Identify the preparation type.
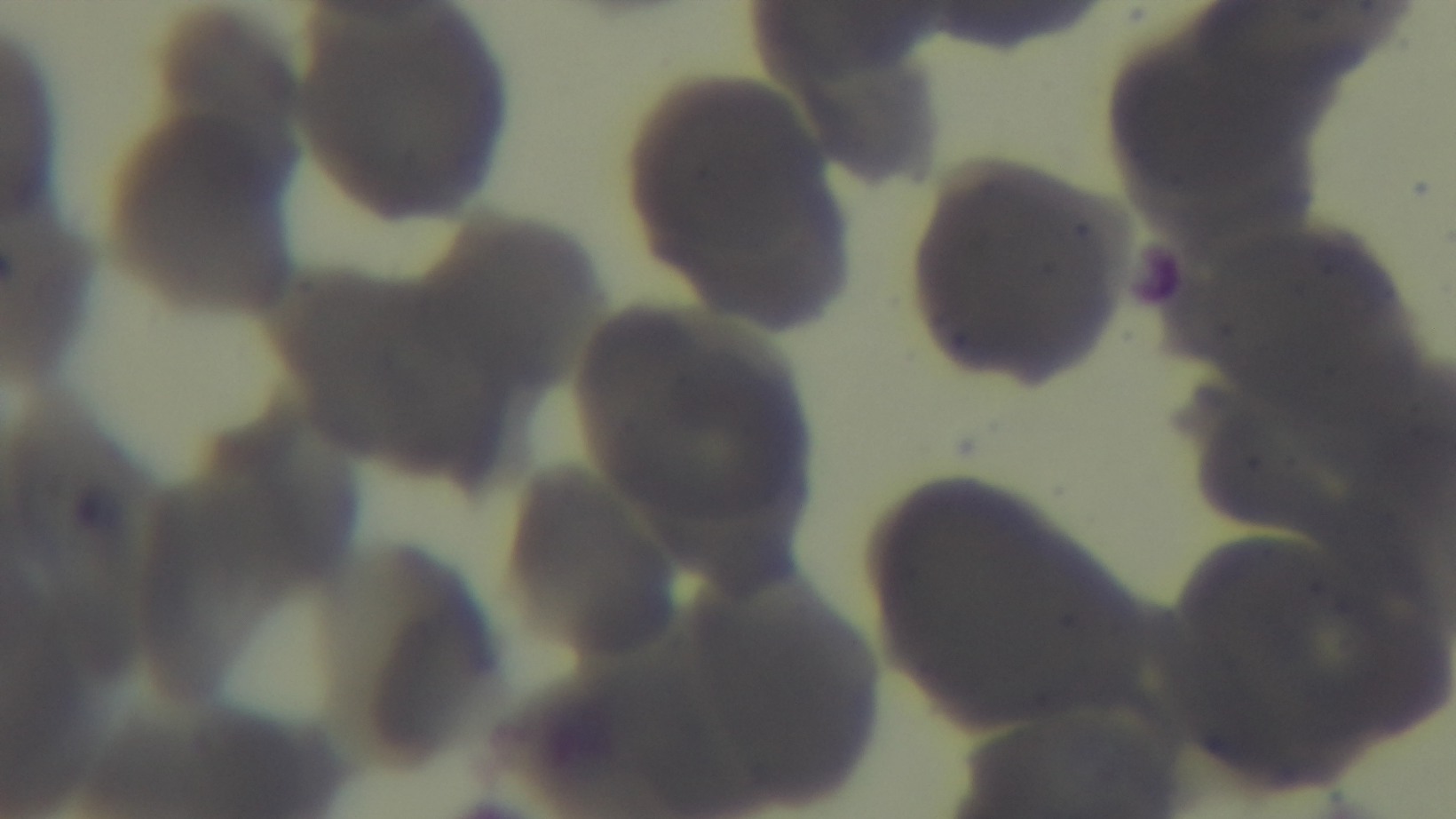

Thin.

capture = mounted 4K digital camera
malaria status = negative
objective = 100x oil immersion
modality = light microscopy
field of view = one from the slide
stain = Giemsa